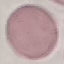 Result: no malaria parasites seen. Thin blood film. Photographed with a smartphone camera at the microscope eyepiece. Giemsa-stained preparation. Cell patch, automatically extracted from a larger field of view and resized to 64 × 64 pixels.